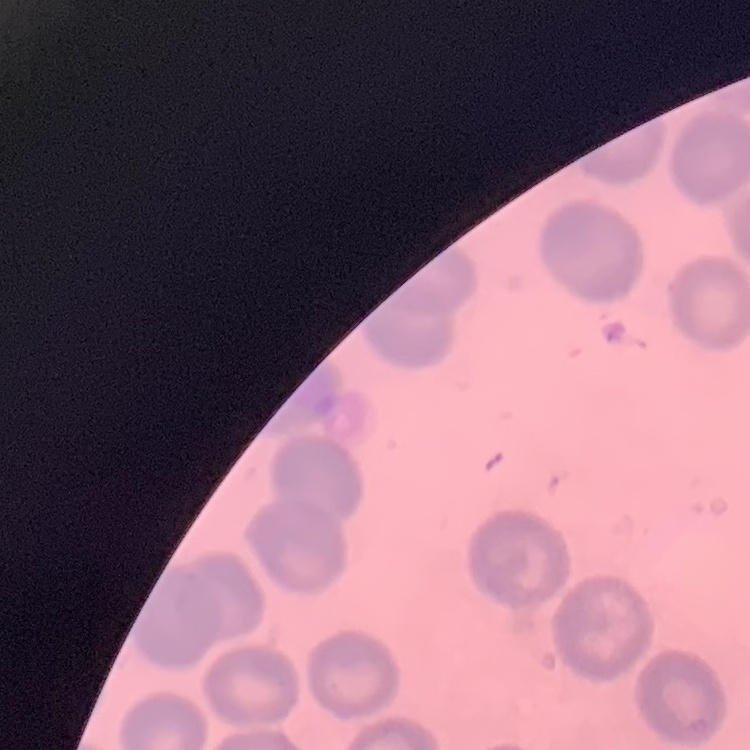 The red blood cells show no rouleaux formation. Thin blood film. One tile cut from a larger photomicrograph. Stained with either Field's or Giemsa.